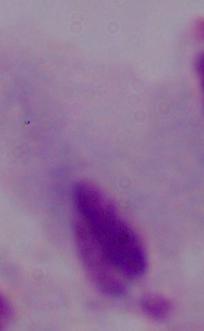
Photomicrograph. 1000x magnification. A trichomonad is shown.